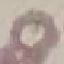
{
  "result": "no malaria parasites detected",
  "stain": "Giemsa",
  "capture": "smartphone camera at the microscope eyepiece",
  "image_type": "cell patch, automatically extracted from a larger field of view and resized to 64 × 64 pixels",
  "preparation": "thin blood film"
}